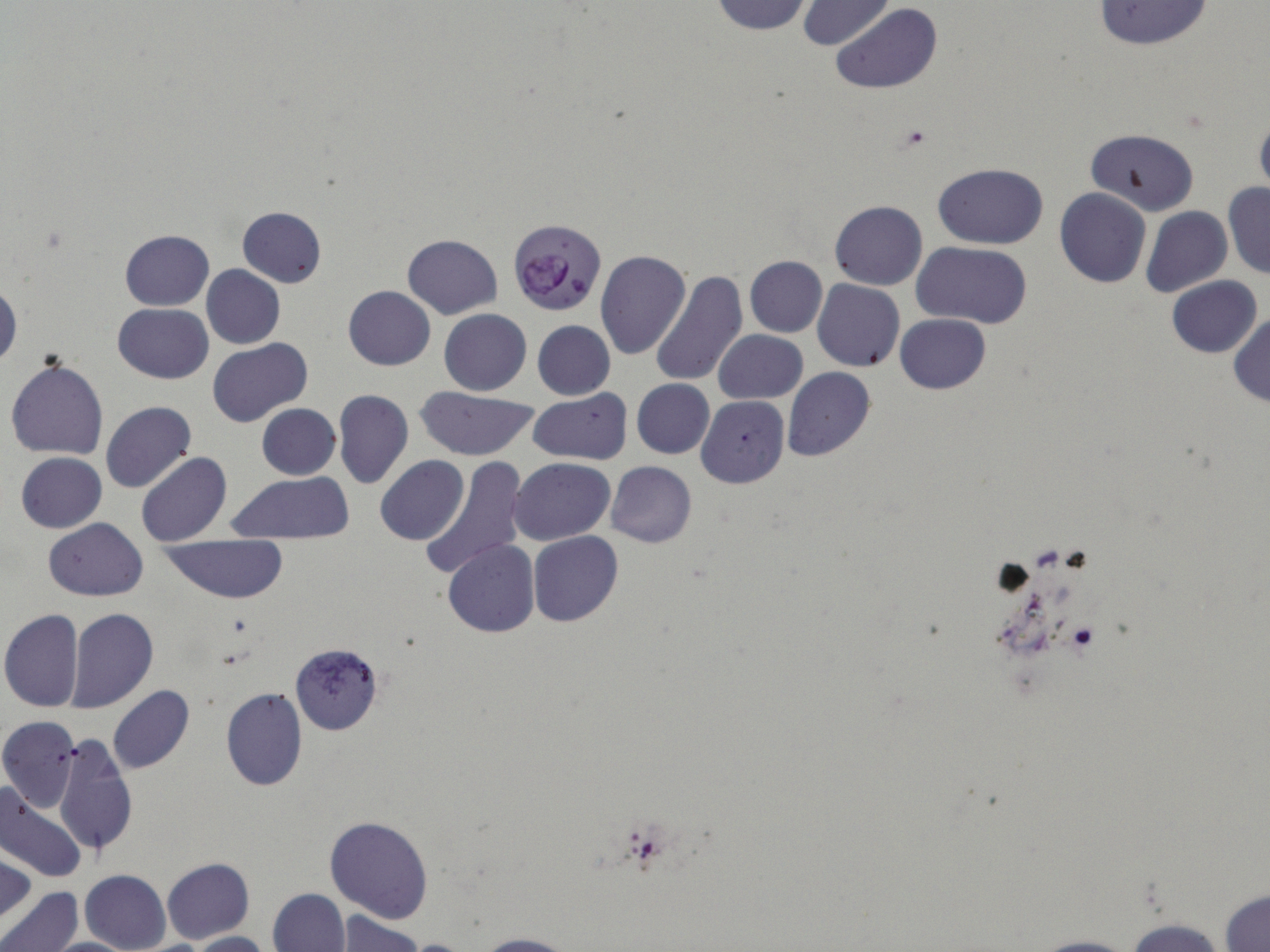
slide-level diagnosis = Plasmodium falciparum
modality = light microscopy
stain = May-Grünwald-Giemsa
image size = 1270×952 pixels
magnification = 1000x
field of view = one of a larger specimen
preparation = thin blood film
uninfected red blood cell locations = approximate bounding boxes as (x1, y1, x2, y2) in pixels: (710, 0, 813, 36), (798, 0, 895, 50), (1092, 0, 1214, 50), (831, 4, 941, 95), (1255, 113, 1270, 198), (1085, 127, 1199, 215), (933, 164, 1048, 248), (1223, 182, 1270, 279), (1054, 188, 1151, 288), (829, 200, 926, 290), (1142, 206, 1233, 297), (237, 207, 326, 287), (120, 230, 213, 311), (404, 234, 502, 319), (914, 242, 1032, 328), (594, 251, 691, 359), (744, 256, 827, 337), (201, 264, 284, 349), (649, 270, 749, 387), (1167, 276, 1261, 358), (1, 279, 21, 370), (814, 280, 905, 371), (343, 285, 435, 369), (112, 303, 213, 383), (440, 309, 531, 395), (1229, 312, 1270, 407), (895, 313, 990, 394), (533, 321, 615, 399), (714, 329, 806, 404), (208, 339, 313, 428), (6, 359, 108, 459), (783, 367, 875, 462), (630, 379, 714, 458), (416, 386, 540, 461), (528, 389, 632, 464), (333, 390, 413, 490), (697, 396, 789, 488), (100, 401, 197, 493), (257, 403, 340, 479), (245, 405, 347, 541), (16, 452, 106, 532), (137, 453, 232, 546), (420, 455, 528, 580), (376, 456, 469, 544), (510, 458, 615, 544), (605, 461, 697, 548), (227, 472, 357, 542), (43, 519, 147, 600), (528, 531, 623, 627), (160, 535, 289, 603), (444, 540, 540, 638), (66, 608, 158, 713), (0, 609, 84, 712), (289, 642, 384, 735), (108, 686, 194, 774), (220, 687, 307, 791), (0, 716, 80, 812), (54, 735, 137, 858), (0, 784, 86, 883), (324, 815, 434, 925), (0, 851, 36, 927), (161, 858, 255, 944), (79, 870, 171, 952), (0, 885, 82, 952), (266, 888, 349, 952), (1219, 888, 1269, 951), (329, 911, 425, 952), (1121, 917, 1233, 952), (184, 931, 272, 952), (475, 933, 577, 952), (1023, 935, 1148, 952), (42, 937, 140, 951)
Plasmodium falciparum-infected red blood cell locations = approximate bounding boxes as (x1, y1, x2, y2) in pixels: (507, 218, 609, 319)